Assess this cell for malaria.
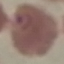

It is parasitized.

stain = Giemsa
preparation = thin blood film
image type = automatically extracted cell patch, resized to 64 × 64 pixels
capture = smartphone camera at the microscope eyepiece